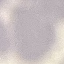

Result: no malaria parasites detected. Thin blood smear. Giemsa-stained preparation. Acquired by smartphone through the microscope eyepiece. Automatically extracted cell patch, resized to 64 × 64 pixels.